Give the extent of all Plasmodium malariae-infected red blood cells.
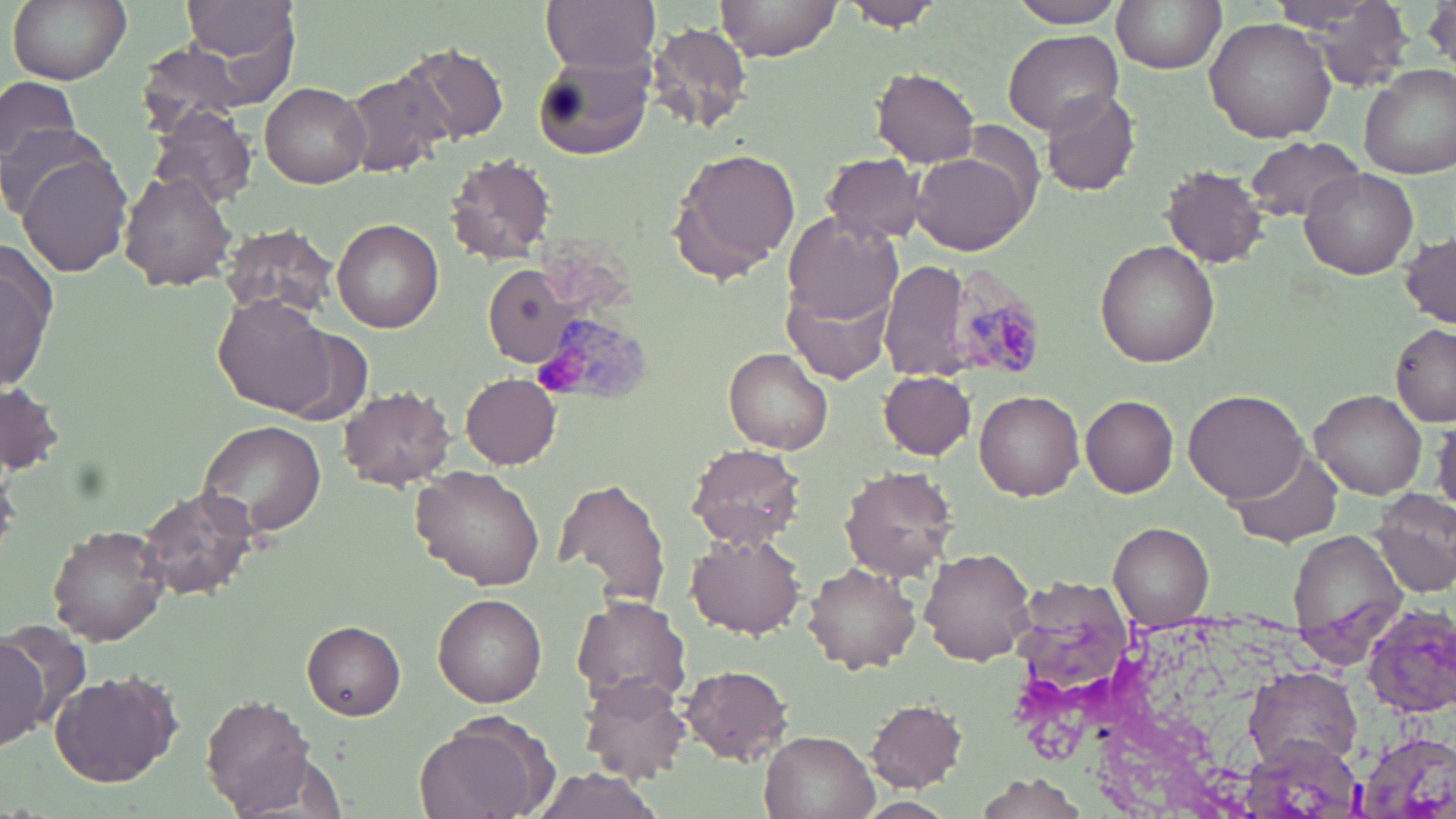

Approximate bounding boxes as (x1,y1)-(x2,y2) corner pairs in pixels.
Plasmodium malariae-infected red blood cells: (948,264)-(1046,378), (535,321)-(655,406).

{
  "slide_level_diagnosis": "Plasmodium malariae",
  "magnification": "1000x",
  "modality": "light microscopy",
  "uninfected_red_blood_cell_locations": "approximate bounding boxes as (x1,y1)-(x2,y2) corner pairs in pixels: (9,0)-(133,85), (541,0)-(661,73), (714,0)-(842,60), (842,0)-(946,30), (1007,0)-(1129,29), (1113,0)-(1225,73), (1278,0)-(1415,76), (183,1)-(298,67), (4,4)-(110,156), (1203,17)-(1336,143), (646,20)-(755,135), (1003,29)-(1125,136), (398,40)-(509,148), (131,42)-(258,140), (531,51)-(656,162), (1358,64)-(1456,180), (870,69)-(982,166), (342,70)-(452,179), (0,75)-(80,171), (261,81)-(370,187), (1040,87)-(1138,195), (147,106)-(260,212), (0,119)-(109,223), (1246,136)-(1361,225), (673,148)-(804,274), (913,149)-(1031,256), (822,152)-(928,243), (15,153)-(134,277), (445,154)-(557,265), (1161,165)-(1269,267), (1300,167)-(1420,279), (120,170)-(237,291), (783,213)-(904,326), (333,218)-(444,332), (219,223)-(340,319), (1400,231)-(1455,327), (1096,241)-(1220,368), (0,242)-(57,393), (881,258)-(976,382), (483,266)-(576,364), (783,281)-(893,383), (212,295)-(344,418), (1391,324)-(1456,429), (725,348)-(834,455), (879,371)-(975,458), (460,373)-(562,469), (0,384)-(65,474), (337,385)-(456,490), (1183,388)-(1310,503), (974,389)-(1084,500), (1309,390)-(1428,498), (1082,396)-(1179,497), (1432,417)-(1456,518), (195,420)-(326,540), (686,442)-(805,548), (1228,445)-(1344,547), (413,465)-(548,591), (840,465)-(959,582), (555,475)-(672,612), (138,486)-(259,597), (1371,492)-(1456,598), (47,523)-(169,645), (1109,523)-(1214,622), (1286,529)-(1409,660), (686,533)-(806,638), (920,545)-(1035,665), (805,561)-(922,673), (433,594)-(547,708), (571,594)-(692,712), (1360,600)-(1456,718), (303,620)-(406,720), (0,635)-(47,747), (680,663)-(797,764), (1245,667)-(1361,777), (51,669)-(180,787), (578,674)-(691,785), (204,694)-(316,813), (864,697)-(968,792), (415,712)-(558,819), (1355,730)-(1456,819), (760,731)-(877,819), (1245,734)-(1364,819), (527,767)-(665,817), (976,774)-(1082,818), (853,795)-(956,818)",
  "preparation": "thin blood smear",
  "stain": "May-Grünwald-Giemsa",
  "image_size": "1456×819 pixels",
  "field_of_view": "single"
}